Identify the cell.
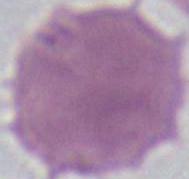
An erythrocyte.

Summary:
  - Modality: photomicrograph
  - Magnification: 1000x